Assess this cell for malaria.
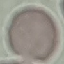
It is uninfected.

Summary:
  - Preparation: thin blood smear
  - Stain: Giemsa
  - Capture: smartphone camera at the microscope eyepiece
  - Image type: cell patch, automatically extracted from a larger field of view and resized to 64 × 64 pixels